Assess this cell for malaria.
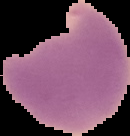

It is parasitized.

From a thin blood film. Image is 130×136 pixels. Cell region segmented out of the field of view; the surrounding area is masked to black.